Assess the morphology of the red blood cells.
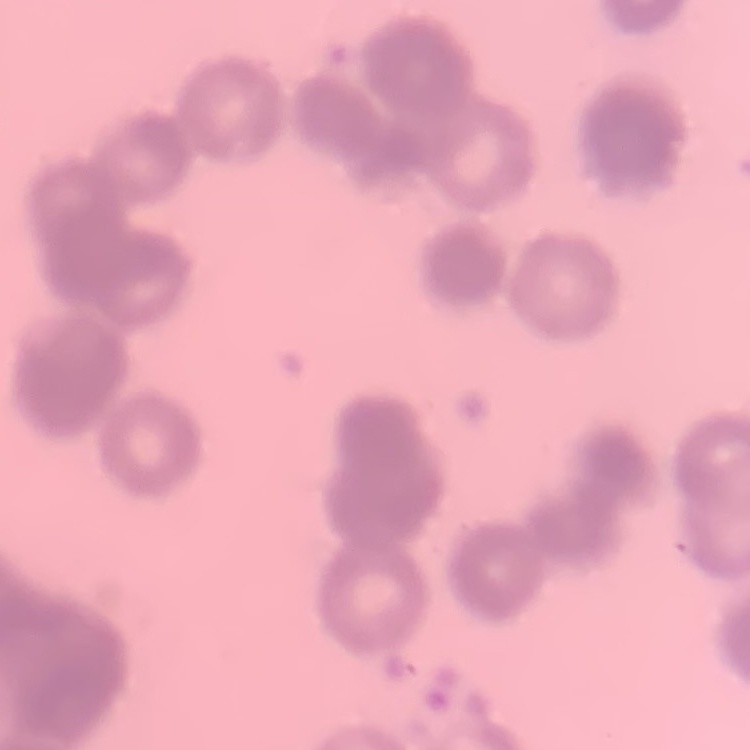

Rouleaux formation.

preparation = thin peripheral smear
stain = Field's or Giemsa
image type = one tile cut from a larger photomicrograph